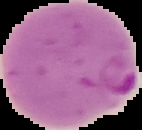 Image is 142×130 pixels. Cell region segmented out of the field of view; the surrounding area is masked to black. From a thin blood film. Malaria status: parasitized.